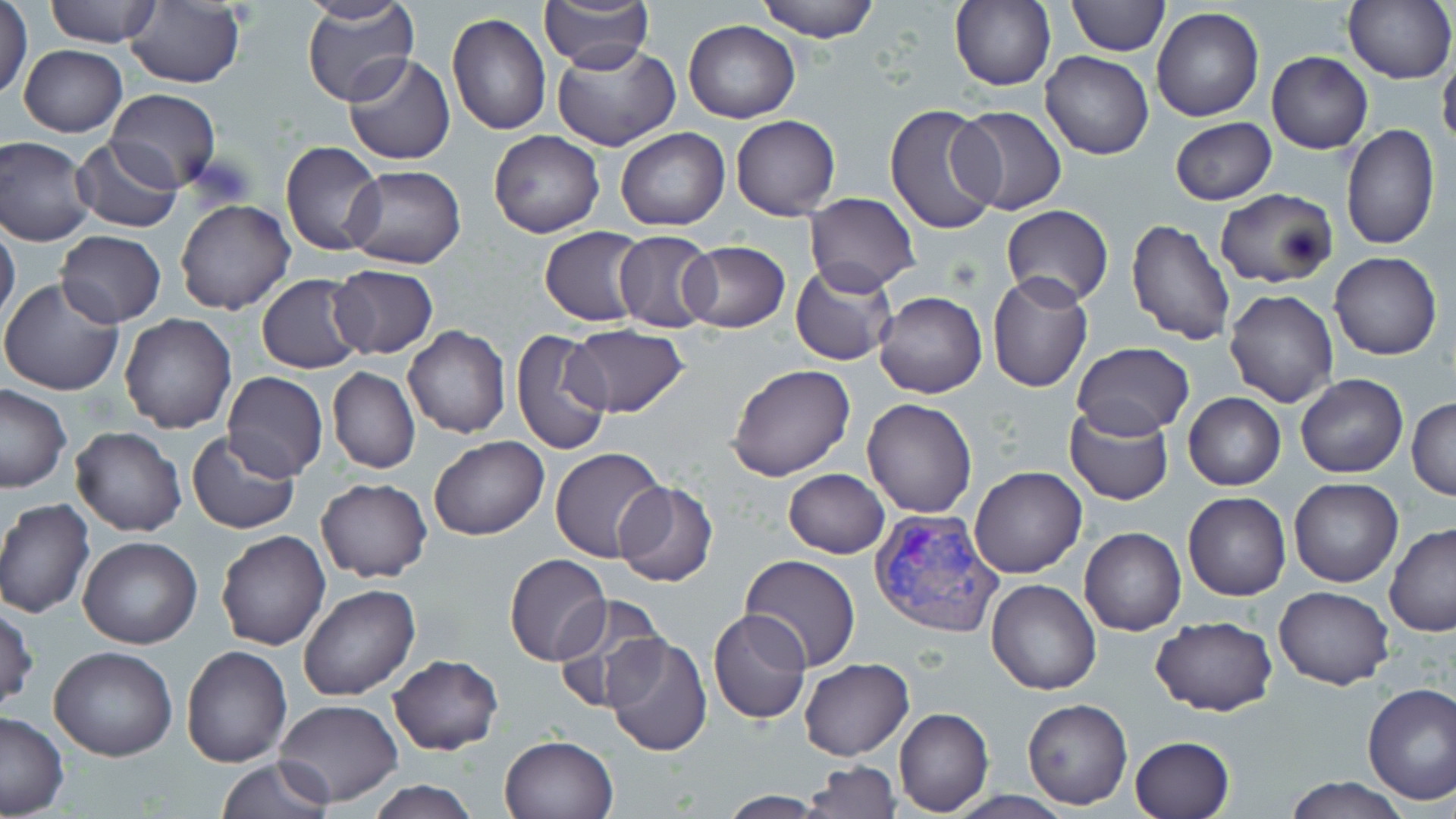
Summary:
  - Coordinate format: approximate bounding boxes as (x1, y1, x2, y2) in pixels
  - Uninfected red blood cell locations: (45, 0, 161, 47), (301, 0, 418, 109), (538, 0, 653, 71), (756, 0, 880, 43), (1066, 0, 1169, 56), (948, 1, 1055, 90), (0, 2, 33, 101), (124, 2, 245, 89), (1343, 2, 1456, 84), (1151, 7, 1263, 122), (446, 11, 552, 137), (684, 20, 800, 123), (550, 41, 680, 151), (19, 43, 126, 137), (1267, 51, 1372, 153), (1438, 51, 1456, 153), (1041, 52, 1153, 160), (344, 53, 454, 166), (107, 89, 220, 190), (885, 104, 1003, 236), (951, 105, 1068, 215), (731, 116, 841, 220), (1170, 118, 1277, 205), (1341, 123, 1438, 248), (616, 128, 730, 231), (488, 130, 605, 238), (0, 135, 96, 246), (71, 135, 185, 234), (281, 141, 385, 255), (342, 164, 466, 270), (1214, 187, 1338, 288), (803, 192, 919, 293), (174, 200, 295, 316), (1000, 205, 1114, 308), (1126, 219, 1237, 347), (0, 222, 21, 332), (539, 226, 650, 326), (613, 230, 718, 332), (56, 231, 166, 326), (679, 240, 790, 333), (1330, 251, 1442, 360), (791, 263, 898, 366), (328, 265, 437, 359), (987, 273, 1093, 393), (257, 274, 367, 374), (0, 277, 123, 395), (1224, 287, 1340, 408), (874, 292, 986, 397), (118, 314, 237, 433), (563, 324, 690, 417), (403, 325, 510, 439), (511, 328, 614, 456), (1071, 342, 1196, 437), (726, 364, 857, 482), (328, 367, 420, 474), (222, 371, 328, 481), (1295, 374, 1408, 478), (0, 383, 71, 492), (1184, 392, 1286, 490), (1406, 396, 1455, 501), (862, 397, 977, 518), (1064, 405, 1174, 505), (69, 426, 186, 537), (187, 429, 300, 534), (429, 435, 548, 540), (550, 447, 669, 564), (971, 466, 1086, 579), (783, 469, 890, 559), (315, 477, 432, 583), (1288, 478, 1403, 587), (614, 481, 719, 586), (1183, 493, 1291, 601), (0, 498, 95, 619), (1384, 524, 1456, 636), (1079, 527, 1186, 636), (216, 530, 330, 650), (78, 536, 202, 650), (505, 554, 610, 665), (739, 555, 861, 672), (985, 578, 1102, 694), (297, 583, 421, 700), (1273, 586, 1395, 690), (551, 593, 668, 713), (0, 600, 37, 716), (709, 608, 812, 726), (1150, 615, 1278, 715), (603, 633, 713, 756), (49, 644, 178, 762), (180, 644, 294, 766), (389, 655, 503, 754), (799, 658, 914, 760), (1361, 682, 1456, 805), (1022, 698, 1132, 810), (274, 699, 403, 805), (894, 707, 993, 816), (0, 710, 67, 818), (499, 734, 619, 819), (1130, 734, 1234, 819), (215, 756, 336, 819), (805, 760, 900, 818), (1282, 776, 1413, 818), (366, 778, 479, 818), (716, 792, 830, 818)
  - Plasmodium vivax-infected red blood cell locations: (868, 507, 1003, 641)
  - Slide-level diagnosis: Plasmodium vivax
  - Modality: light microscopy
  - Image size: 1456×819 pixels
  - Stain: May-Grünwald-Giemsa
  - Preparation: thin blood film
  - Magnification: 1000x
  - Field of view: one of a larger specimen